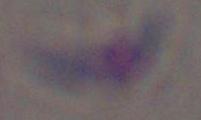 1000x magnification. Toxoplasma gondii is seen. Photomicrograph.